State which parasite is depicted.
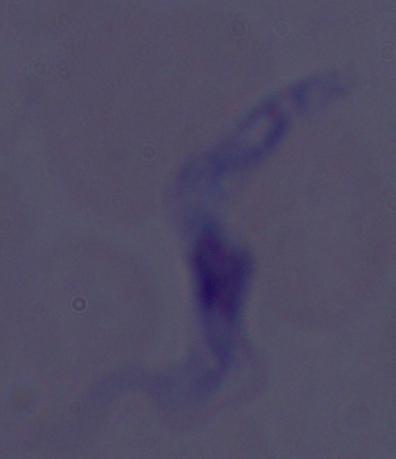
A trypanosome.

Micrograph. Captured at 1000x magnification.